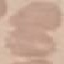

result = no malaria parasites detected
image type = cell patch, automatically extracted from a larger field of view and resized to 64 × 64 pixels
stain = Giemsa
preparation = thin smear
capture = smartphone through the microscope eyepiece